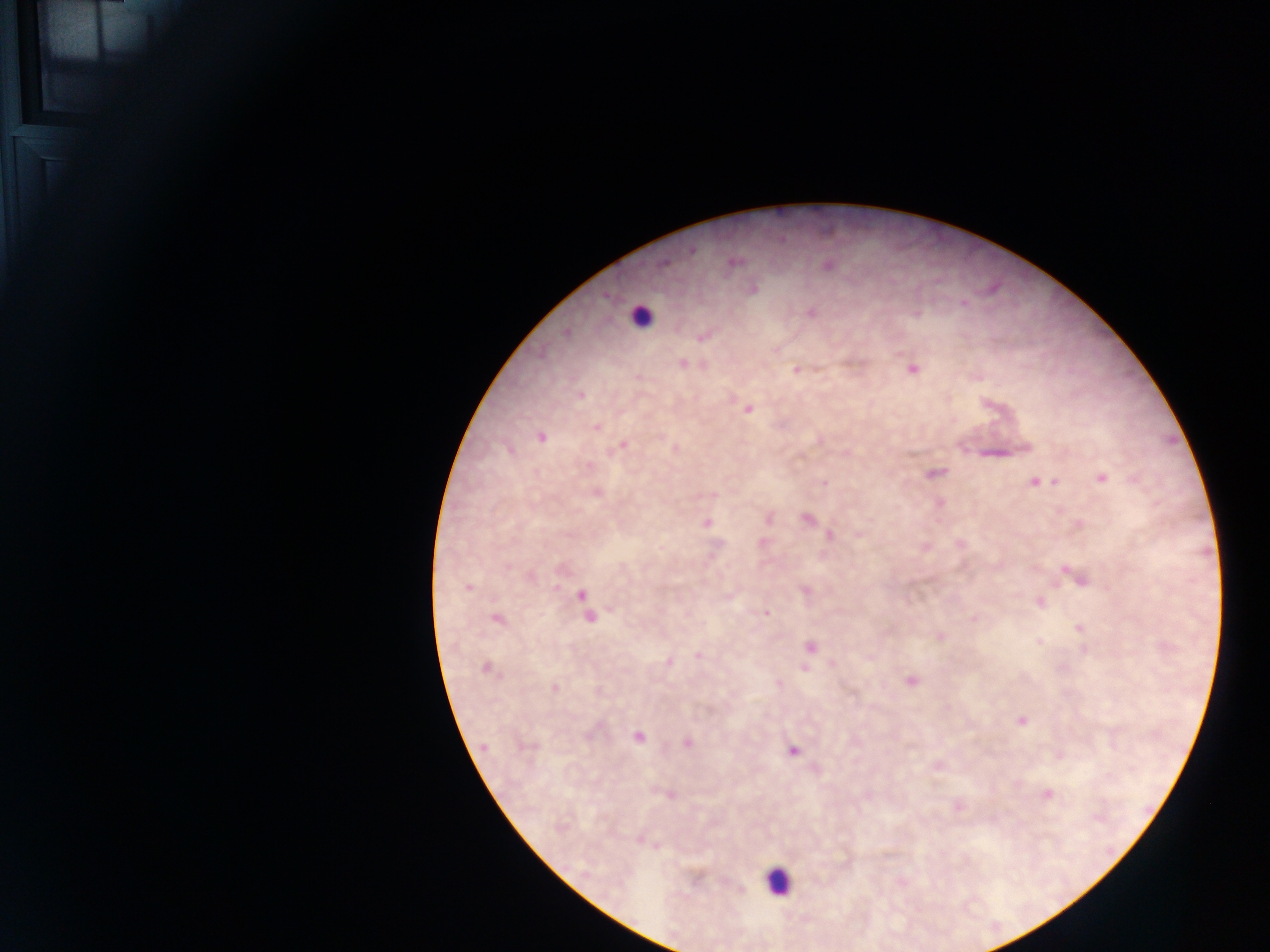

country = Ghana
capture = mobile-phone photograph through a microscope
field of view = single
leukocyte locations = approximate centers as {x, y} in pixels: {641, 316}, {778, 881}
image size = 1270×952 pixels
preparation = thick blood film
Plasmodium parasite locations = approximate centers as {x, y} in pixels: {692, 251}, {734, 262}, {664, 263}, {829, 266}, {753, 289}, {963, 303}, {812, 312}, {566, 333}, {702, 338}, {682, 363}, {913, 369}, {796, 370}, {581, 396}, {748, 410}, {597, 428}, {541, 437}, {619, 446}, {510, 450}, {935, 473}, {1102, 478}, {1038, 482}, {1048, 482}, {824, 483}, {597, 493}, {769, 519}, {807, 519}, {707, 523}, {829, 535}, {763, 542}, {1078, 578}, {469, 586}, {581, 595}, {1040, 603}, {767, 613}, {590, 618}, {497, 619}, {973, 619}, {1080, 628}, {940, 637}, {1040, 642}, {810, 648}, {697, 656}, {669, 662}, {805, 667}, {486, 668}, {910, 681}, {779, 683}, {555, 688}, {1020, 721}, {637, 737}, {687, 743}, {529, 746}, {483, 747}, {793, 750}, {669, 795}, {1047, 795}, {958, 807}